Classify this cell by malaria status.
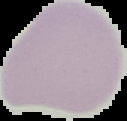

It is uninfected.

{
  "image_type": "cell region segmented out of the field of view; surrounding area masked to black",
  "preparation": "thin blood film",
  "image_size": "127×121 pixels"
}